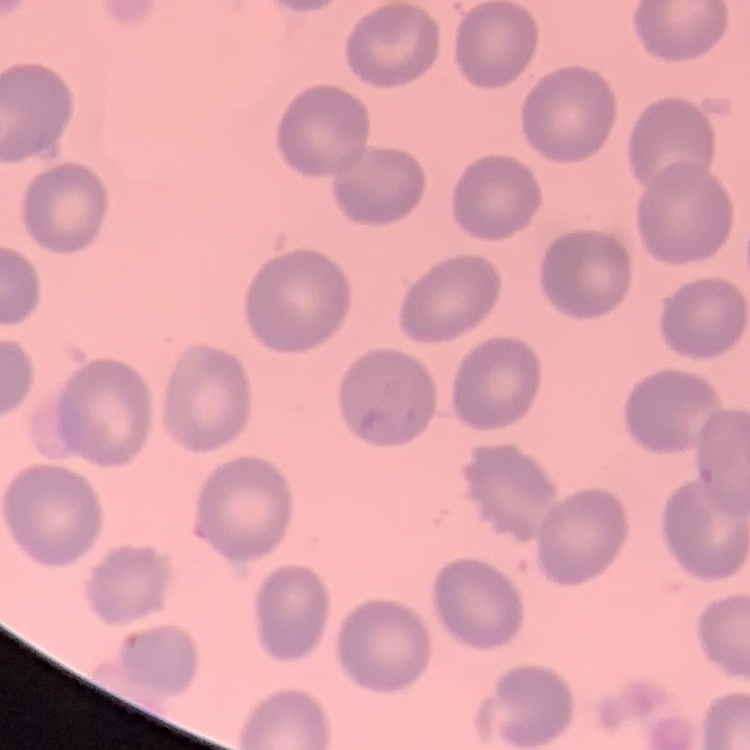

Summary:
  - Red blood cell morphology: no rouleaux formation
  - Image type: square crop of a larger photomicrograph
  - Stain: Field's or Giemsa
  - Preparation: thin blood smear